Assess this cell for malaria.
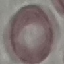
It is uninfected.

Summary:
  - Capture: smartphone through the microscope eyepiece
  - Image type: automatically extracted cell patch, resized to 64 × 64 pixels
  - Preparation: thin smear
  - Stain: Giemsa